Identify the parasite.
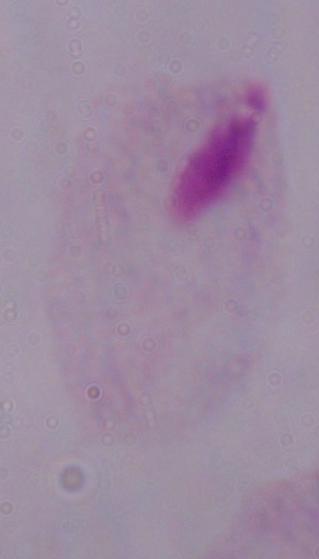

This is a trichomonad.

Summary:
  - Magnification: 1000x
  - Modality: photomicrograph